Assess the morphology of the erythrocytes.
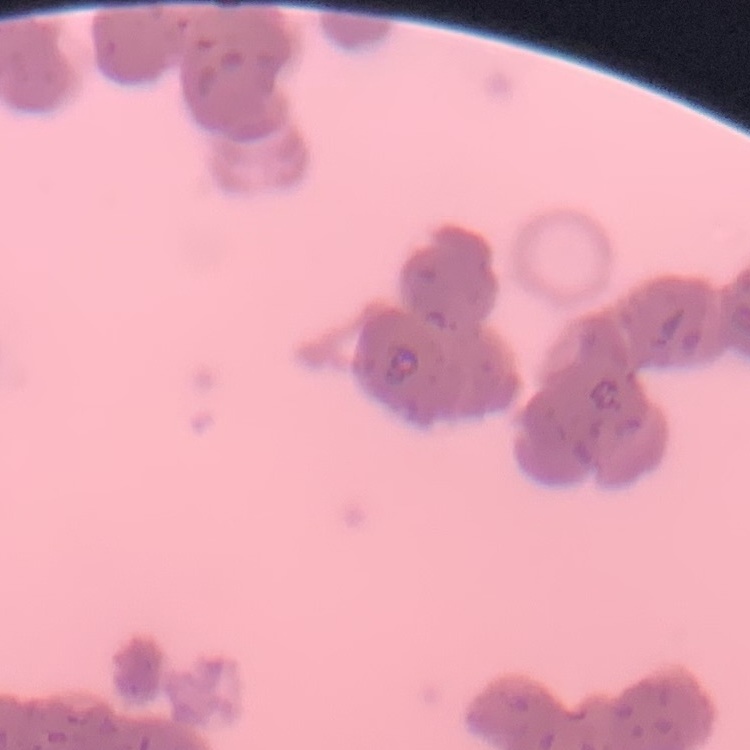
They show rouleaux formation.

image type = one tile cut from a larger photomicrograph
stain = Field's or Giemsa
preparation = thin blood film